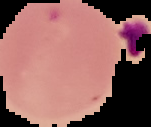
{
  "preparation": "thin blood smear",
  "image_type": "segmented cell region on a black background",
  "malaria_status": "uninfected",
  "image_size": "151×127 pixels"
}